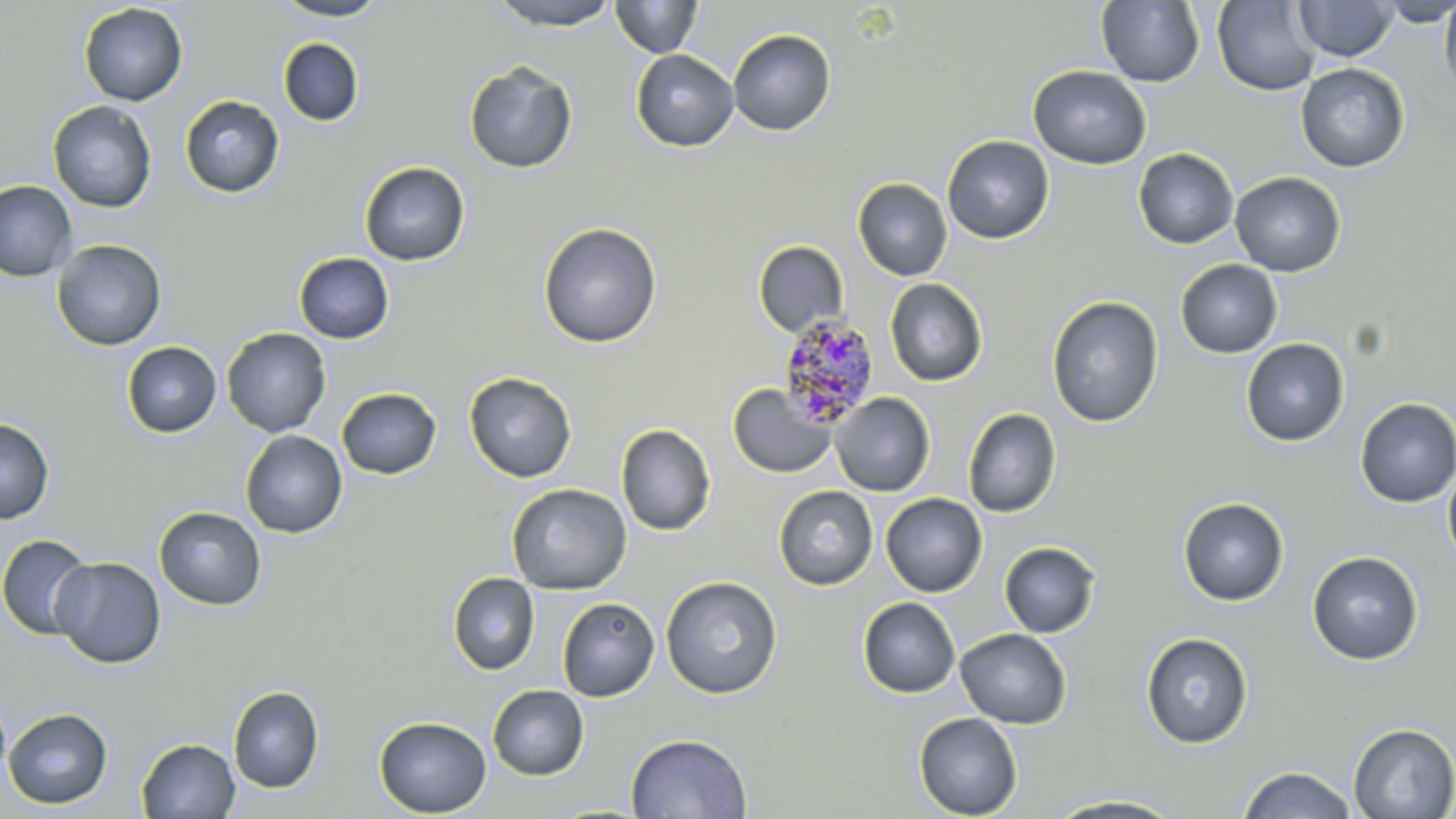
slide-level diagnosis = Plasmodium malariae
uninfected red blood cell locations = approximate bounding boxes as (x1, y1, x2, y2) in pixels: (270, 0, 391, 21), (486, 0, 621, 30), (1095, 0, 1205, 87), (1293, 0, 1397, 62), (1373, 0, 1456, 27), (1439, 0, 1456, 96), (611, 1, 703, 58), (1212, 1, 1321, 95), (78, 2, 188, 106), (727, 28, 836, 136), (278, 38, 364, 127), (630, 48, 739, 152), (463, 60, 578, 175), (1295, 63, 1410, 173), (1028, 65, 1151, 169), (180, 94, 285, 198), (47, 101, 157, 213), (942, 135, 1054, 244), (1133, 147, 1239, 249), (358, 161, 471, 267), (1229, 171, 1346, 276), (852, 178, 952, 281), (0, 180, 78, 282), (537, 222, 662, 349), (51, 239, 167, 351), (753, 240, 849, 338), (293, 252, 394, 344), (1175, 259, 1283, 358), (884, 278, 988, 386), (1046, 295, 1163, 428), (221, 327, 331, 438), (1241, 338, 1350, 447), (121, 341, 221, 438), (463, 371, 577, 483), (727, 384, 836, 479), (336, 387, 441, 479), (830, 393, 935, 496), (1354, 397, 1456, 507), (963, 408, 1061, 518), (0, 417, 55, 524), (616, 424, 716, 536), (240, 430, 348, 539), (1442, 461, 1456, 571), (507, 483, 632, 595), (773, 485, 878, 590), (881, 493, 987, 597), (1177, 497, 1290, 606), (154, 506, 267, 610), (0, 534, 94, 640), (999, 542, 1101, 638), (1307, 550, 1423, 665), (50, 556, 167, 669), (447, 572, 540, 675), (660, 575, 783, 699), (857, 597, 961, 698), (557, 598, 659, 701), (955, 627, 1072, 729), (1140, 631, 1254, 747), (487, 685, 589, 781), (228, 686, 324, 793), (3, 708, 113, 810), (913, 712, 1023, 819), (374, 716, 491, 817), (1348, 722, 1456, 818), (625, 733, 753, 818), (136, 738, 240, 819), (1236, 765, 1359, 819), (1043, 794, 1190, 817)
field of view = single
Plasmodium malariae-infected red blood cell locations = approximate bounding boxes as (x1, y1, x2, y2) in pixels: (776, 314, 879, 429)
magnification = 1000x
modality = optical microscopy
image size = 1456×819 pixels
stain = May-Grünwald-Giemsa
preparation = thin blood film